Identify the parasite.
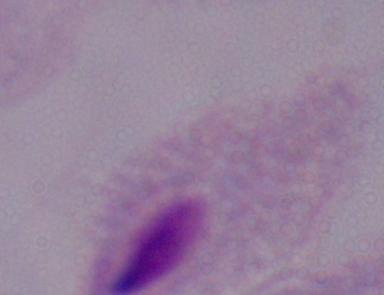

A trichomonad.

Summary:
  - Magnification: 1000x
  - Modality: photomicrograph